Point out each leukocyte.
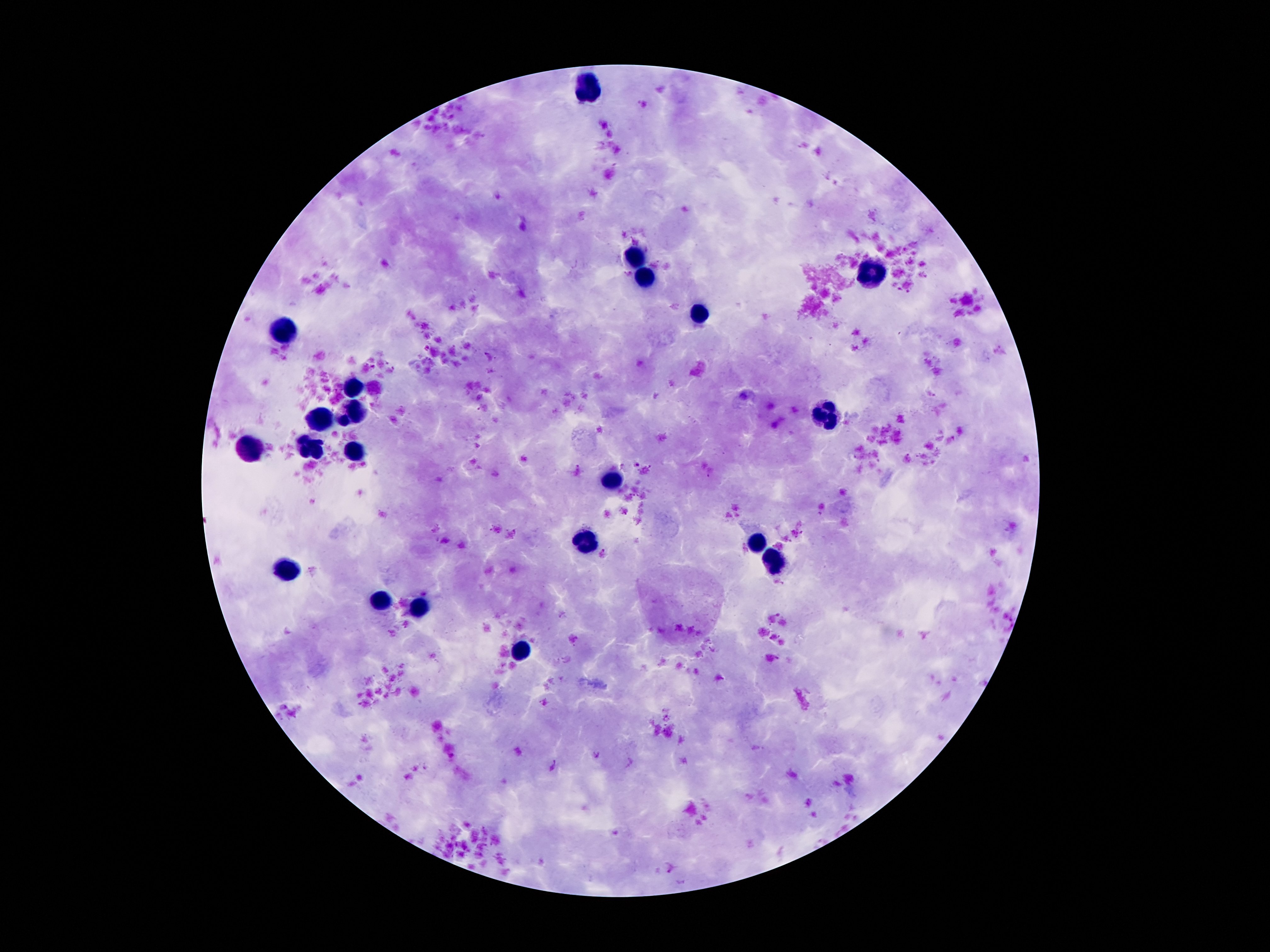

Approximate centers as {x, y} in pixels.
Leukocytes: {589, 88}, {635, 256}, {874, 274}, {643, 280}, {699, 313}, {286, 330}, {355, 386}, {350, 412}, {826, 417}, {321, 419}, {250, 448}, {311, 448}, {355, 451}, {615, 477}, {584, 541}, {757, 541}, {777, 565}, {288, 570}, {380, 600}, {419, 606}, {522, 651}.

Summary:
  - Malaria parasite locations: {426, 348}, {637, 463}, {604, 552}, {779, 614}, {778, 657}
  - Image size: 1270×952 pixels
  - Stain: Giemsa
  - Field of view: one from this slide
  - Patient malaria status: infected with Plasmodium falciparum
  - Magnification: 100x
  - Preparation: thick peripheral-blood smear
  - Capture: smartphone camera through the microscope eyepiece